Evaluate for Plasmodium parasites.
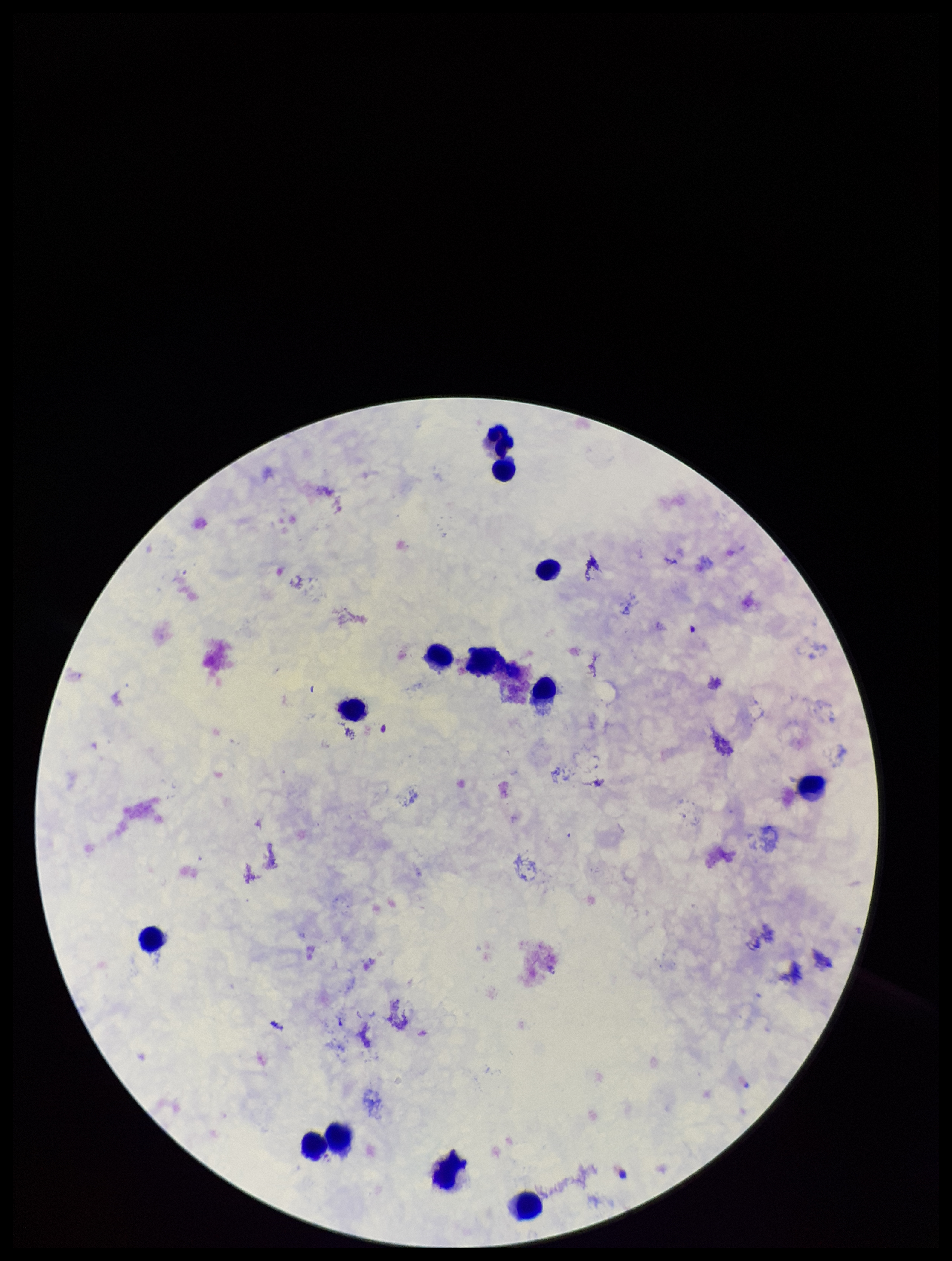
None seen.

Summary:
  - Leukocyte count: 13
  - Patient malaria status: positive
  - Species reported for this patient: Plasmodium falciparum
  - Field of view: one from this slide
  - Parasite count: 0
  - Image size: 952×1261 pixels
  - Stain: Giemsa
  - Preparation: thick smear
  - Capture: smartphone photograph through the microscope eyepiece